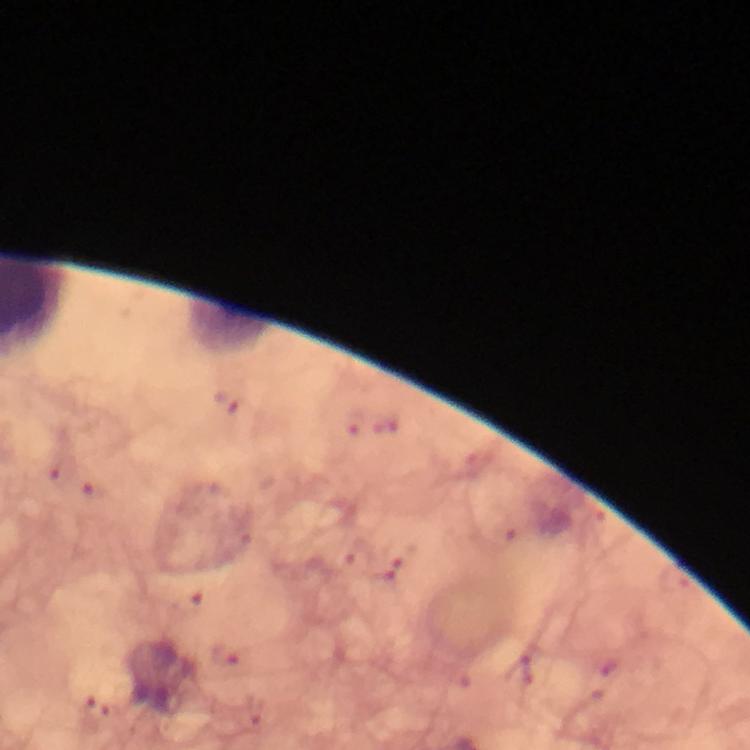 Approximate centers as (x, y) in pixels. Plasmodium parasite locations: (226, 403), (58, 473), (94, 491). Immersion oil applied. Photographed through the microscope with a smartphone camera. Thick blood smear. From a diagnostic examination for malaria. Giemsa stain. 100x magnification. Cropped region of a single field of view. Image is 750×750 pixels.